Classify this cell by malaria status.
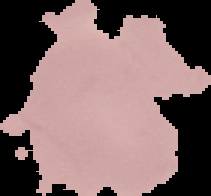

It is uninfected.

Summary:
  - Image type: segmented cell region with the area outside set to black
  - Preparation: thin blood smear
  - Image size: 211×196 pixels